Point out each Plasmodium parasite.
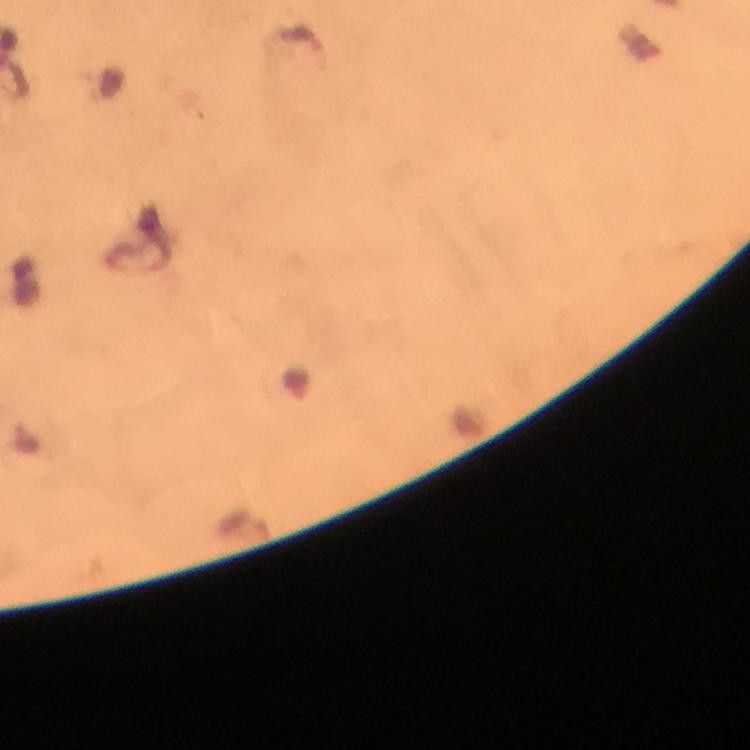

Approximate object centers, in pixels from the top-left corner.
Plasmodium parasites: (x=302, y=41).

{
  "immersion_oil": "used",
  "context": "from a diagnostic examination for malaria",
  "capture": "smartphone photograph through a microscope",
  "magnification": "100x",
  "image_size": "750×750 pixels",
  "preparation": "thick smear",
  "stain": "Giemsa",
  "cropped_from": "a single field of view"
}